Assess this cell for malaria.
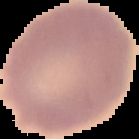

It is uninfected.

From a thin blood film. Cell region segmented out of the field of view; the surrounding area is masked to black. Image is 139×139 pixels.